Name the parasite shown.
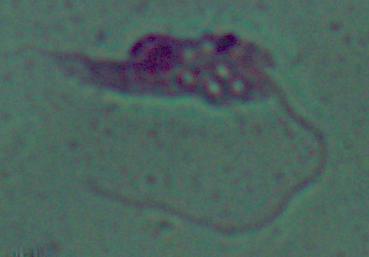

This is Leishmania.

magnification = 1000x
modality = photomicrograph